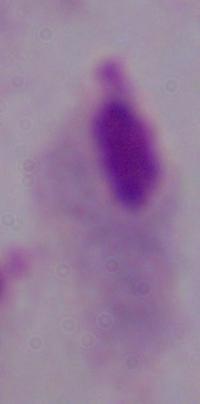

magnification = 1000x
modality = micrograph
identification = trichomonad